Rate the background quality.
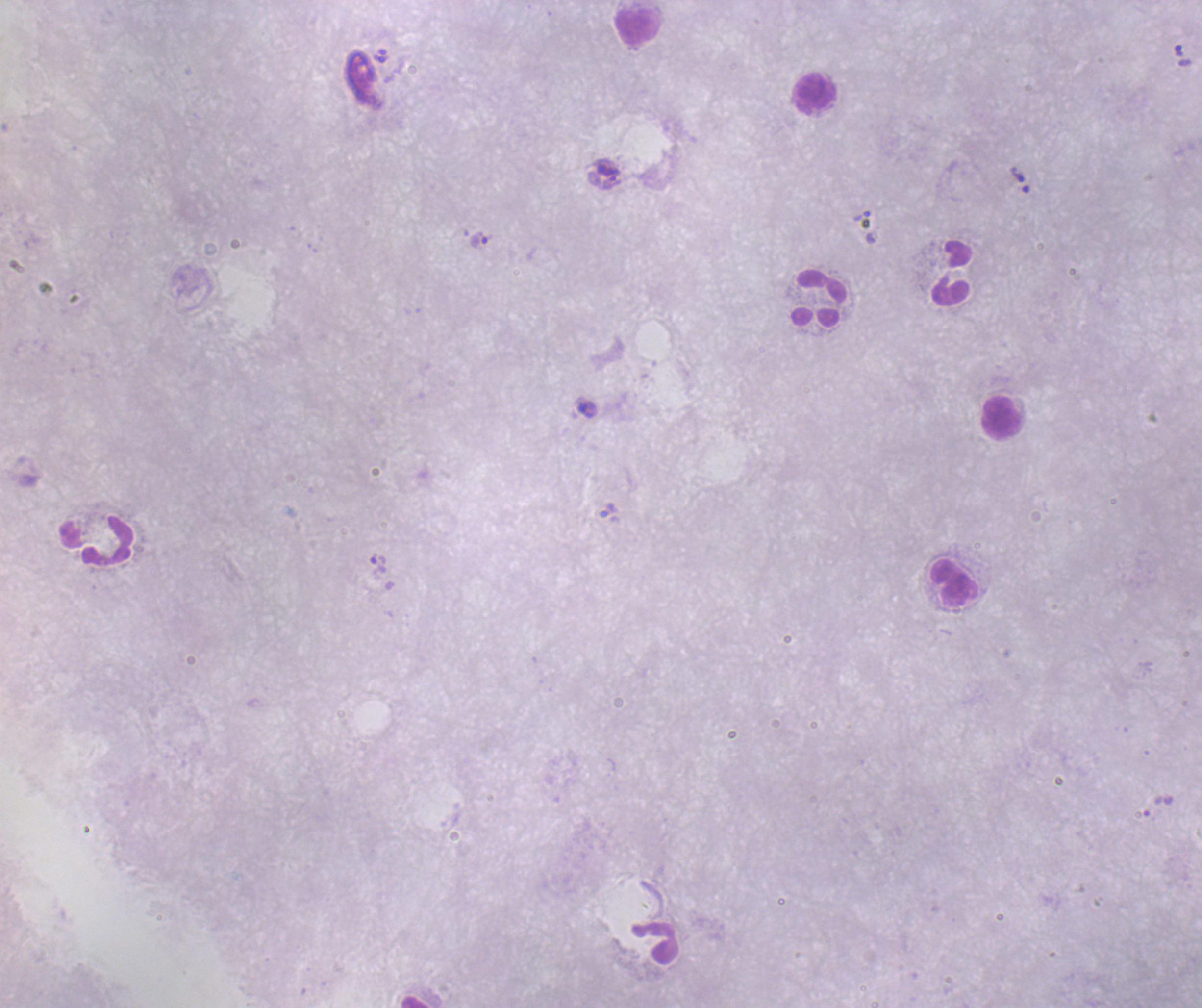
It is poor.

coordinate format = approximate centers as [x, y] in pixels
trophozoite locations = [1179, 51], [1017, 175], [481, 240], [586, 409], [379, 565]
leukocyte locations = [638, 26], [814, 94], [952, 273], [819, 298], [1002, 418], [97, 540], [955, 583]
magnification = 100x
coloration quality = bad
image size = 1202×1008 pixels
field of view = single
result = Plasmodium parasites identified
stain = Romanowsky
context = previously used in an actual diagnosis
preparation = thick blood film